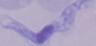
modality = micrograph
magnification = 1000x
identification = trypanosome